Outline each uninfected red blood cell.
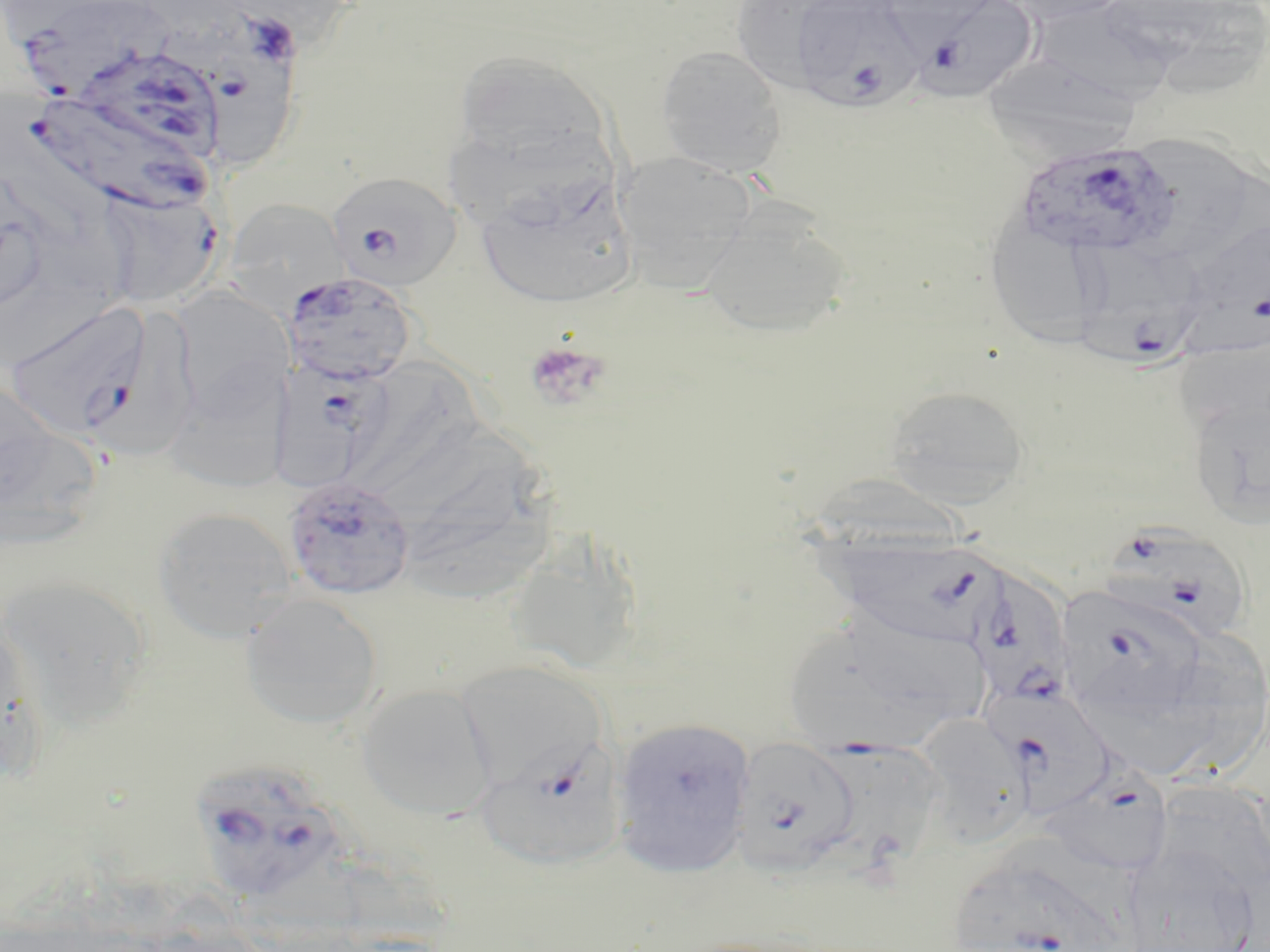

Approximate bounding boxes as (x1,y1)-(x2,y2) corner pairs in pixels.
Uninfected red blood cells: (1002,0)-(1135,25), (737,1)-(825,99), (1171,1)-(1270,98), (1035,10)-(1176,104), (655,45)-(787,177), (453,49)-(611,170), (980,54)-(1142,160), (1123,134)-(1262,262), (611,150)-(757,293), (476,176)-(636,310), (222,198)-(351,316), (27,200)-(145,314), (699,204)-(852,340), (984,216)-(1106,348), (170,286)-(292,419), (1175,326)-(1270,442), (356,357)-(476,486), (163,373)-(291,493), (0,375)-(64,509), (884,385)-(1031,506), (1186,390)-(1270,530), (0,410)-(104,552), (417,461)-(566,610), (153,507)-(297,643), (505,534)-(644,676), (1,575)-(152,724), (240,593)-(383,730), (1189,625)-(1267,784), (0,626)-(52,784), (356,683)-(497,821), (1090,698)-(1232,785), (915,714)-(1035,846), (610,716)-(755,876), (476,741)-(627,873), (1151,779)-(1270,898), (1121,846)-(1261,952).

slide-level diagnosis = Plasmodium falciparum
magnification = 1000x
field of view = single
Plasmodium falciparum-infected red blood cell locations = approximate bounding boxes as (x1,y1)-(x2,y2) corner pairs in pixels: (12,0)-(174,94), (788,0)-(924,110), (911,0)-(1041,103), (170,6)-(302,161), (77,46)-(227,159), (24,91)-(213,217), (1013,141)-(1180,259), (325,170)-(462,292), (95,185)-(224,309), (1179,214)-(1270,345), (1072,240)-(1206,366), (281,271)-(419,386), (4,300)-(156,440), (270,359)-(391,490), (281,475)-(416,602), (1109,523)-(1246,642), (831,532)-(1005,644), (968,564)-(1072,706), (1056,583)-(1209,723), (784,611)-(985,755), (453,659)-(607,799), (989,687)-(1118,822), (731,737)-(860,876), (803,737)-(946,872), (187,757)-(349,904), (1038,764)-(1175,879), (950,848)-(1132,952)
preparation = thin blood film
image size = 1270×952 pixels
modality = light microscopy
stain = May-Grünwald-Giemsa
platelet locations = approximate bounding boxes as (x1,y1)-(x2,y2) corner pairs in pixels: (524,340)-(610,412)